Describe the morphology of the erythrocytes.
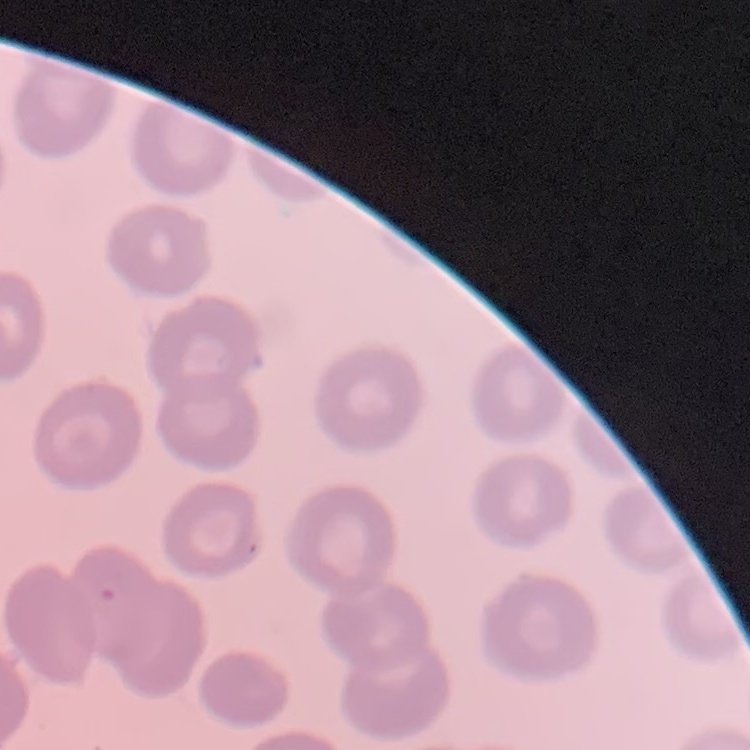
They show no rouleaux formation.

Thin blood smear. One tile cut from a larger photomicrograph. Field's or Giemsa stain.